Assess this cell for malaria.
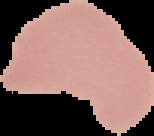
It is uninfected.

Summary:
  - Image type: cell region segmented out of the field of view; surrounding area masked to black
  - Preparation: thin blood film
  - Image size: 154×136 pixels